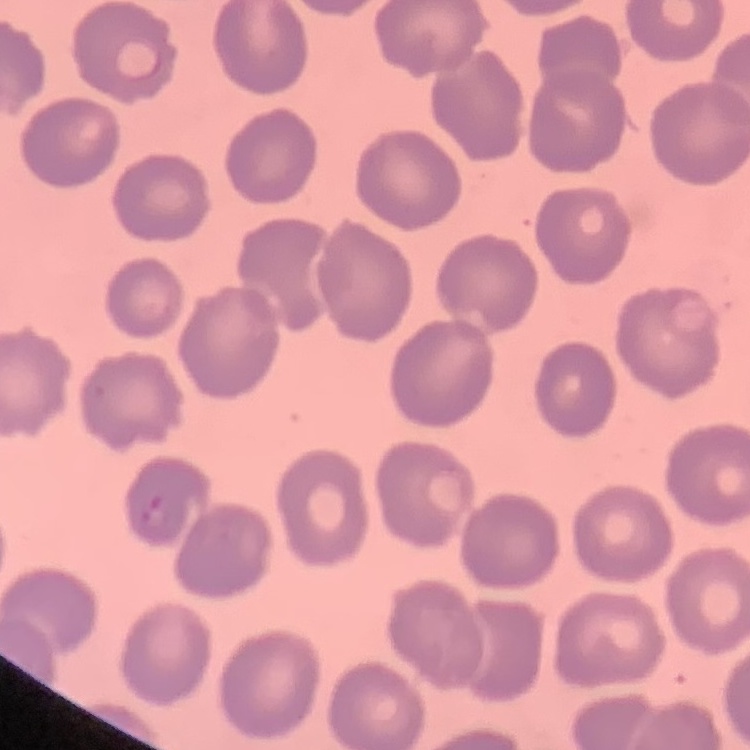
erythrocyte morphology = no rouleaux formation
image type = square crop of a larger photomicrograph
preparation = thin blood film
stain = Field's or Giemsa